Classify this cell by malaria status.
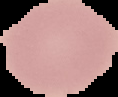
It is uninfected.

The area outside the segmented cell region is set to black. From a thin blood film. Image is 118×97 pixels.